State which parasite is depicted.
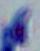

This is Toxoplasma gondii.

Micrograph. Captured at 1000x magnification.